Report the malaria status of this cell.
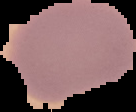
It is uninfected.

preparation = thin blood smear
image size = 136×112 pixels
image type = cell region segmented out of the field of view; surrounding area masked to black